State which cell type is depicted.
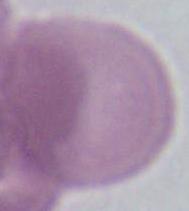

An erythrocyte.

Summary:
  - Modality: photomicrograph
  - Magnification: 1000x